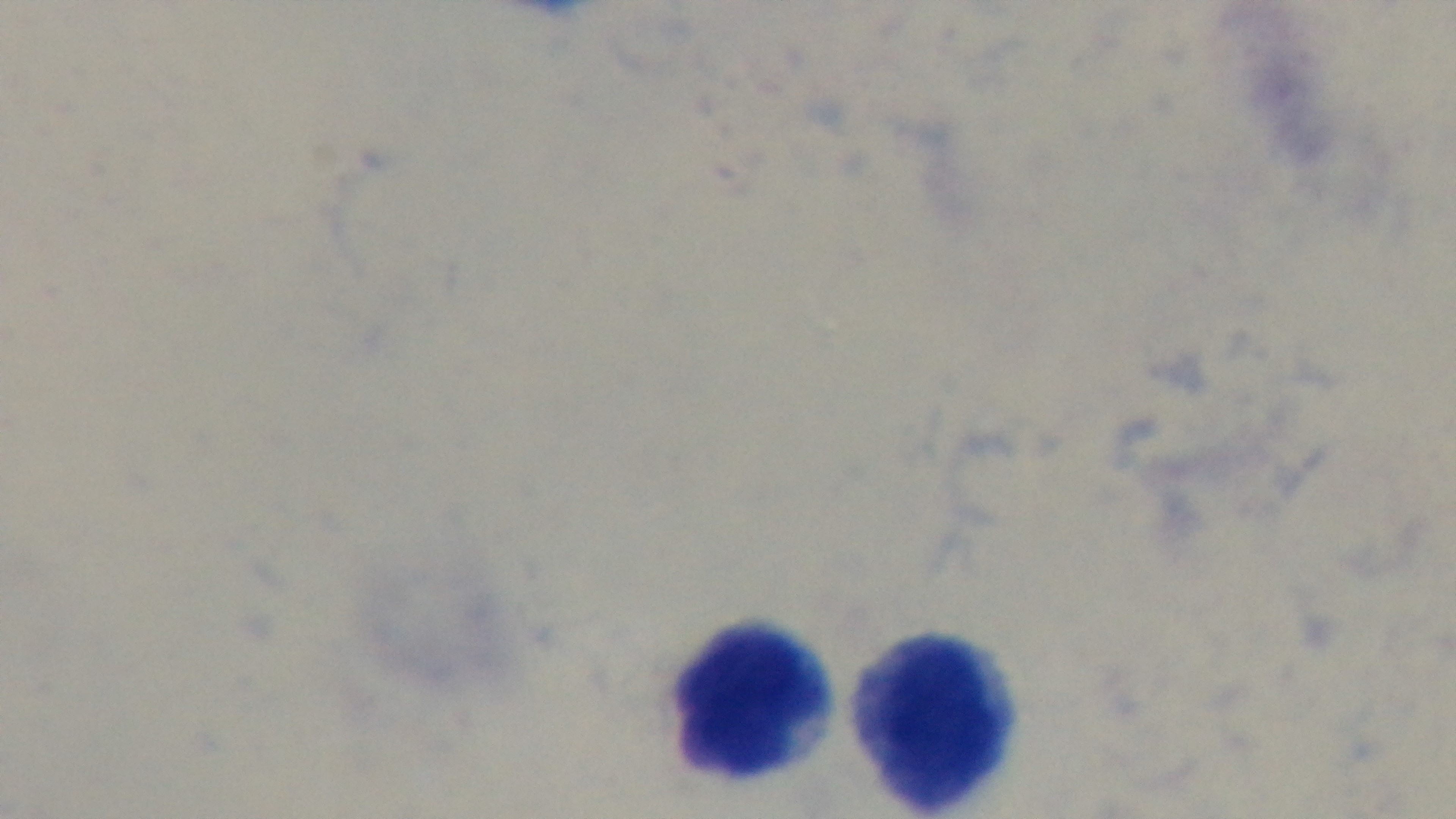
One field from the slide. 100x oil-immersion objective. Light microscopy. Giemsa stain. Malaria status: negative. Mounted 4K digital camera. Preparation: thick smear.